Assess for Plasmodium parasites.
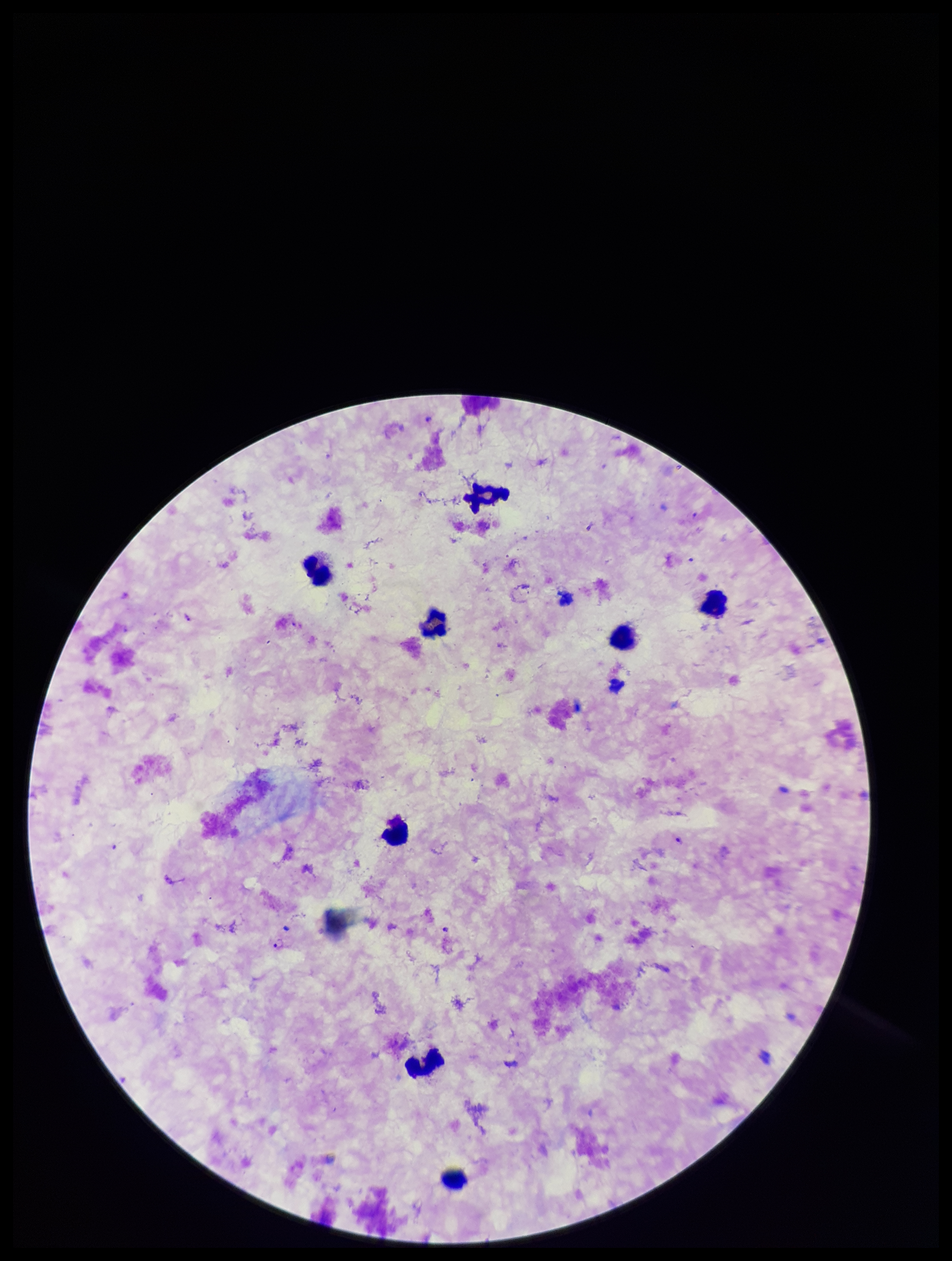
Detected.

Preparation: thick blood smear. Single field of view. Patient malaria status: positive. Smartphone photograph taken through the eyepiece of a microscope. Leukocyte count: 9. Species reported for this patient: Plasmodium falciparum. Image is 952×1261 pixels. Parasite count: 2. Stained with Giemsa.